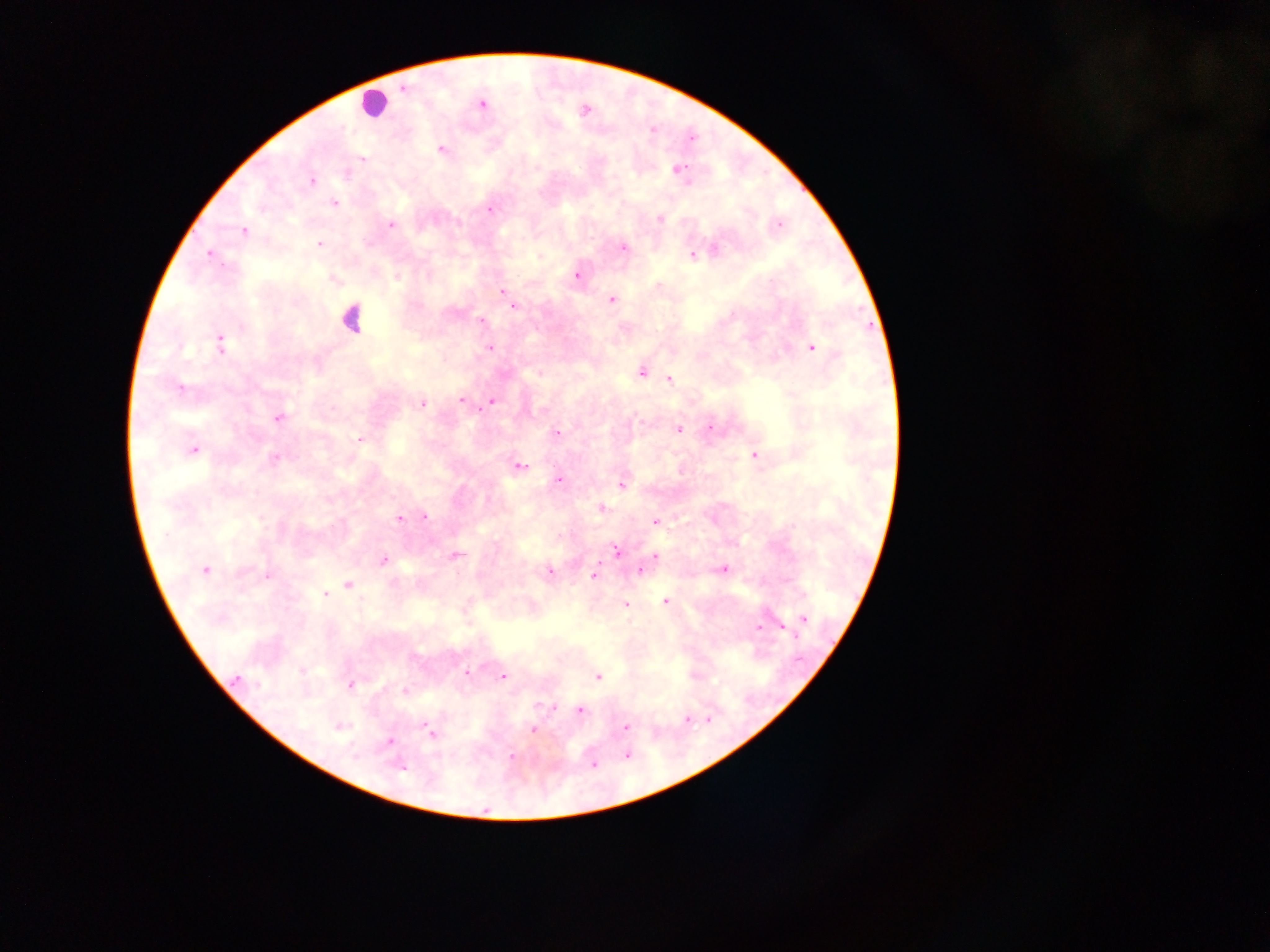
Approximate centers as x y in pixels.
Summary:
  - Leukocyte locations: 371 103; 350 317
  - Malaria parasite locations: 404 87; 481 104; 442 149; 363 160; 680 169; 311 180; 335 204; 490 209; 660 219; 391 224; 778 225; 244 231; 319 243; 623 247; 714 250; 209 254; 692 255; 577 276; 397 278; 503 292; 611 300; 513 307; 480 320; 220 343; 812 347; 490 348; 641 372; 669 379; 180 387; 461 400; 491 401; 422 404; 278 418; 710 428; 679 430; 557 433; 360 439; 193 450; 755 455; 275 458; 520 466; 559 479; 621 484; 602 508; 425 516; 399 517; 656 522; 616 552; 457 554; 656 556; 383 560; 723 569; 205 570; 639 570; 550 572; 268 576; 594 576; 348 585; 325 594; 665 601; 626 605; 804 619; 759 627; 783 628; 796 636; 466 673; 503 676; 598 677; 237 678; 350 685; 405 691; 580 711; 687 719; 427 725; 340 727; 625 727; 533 729; 430 733; 389 742; 627 755; 512 756; 593 764; 401 768
  - Image size: 1270×952 pixels
  - Preparation: thick blood smear
  - Field of view: single
  - Country: Ghana
  - Capture: mobile-phone photograph through a microscope